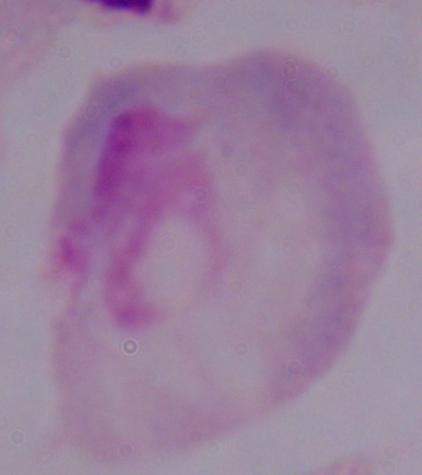
modality = micrograph
magnification = 1000x
identification = trichomonad